Describe the morphology of the erythrocytes.
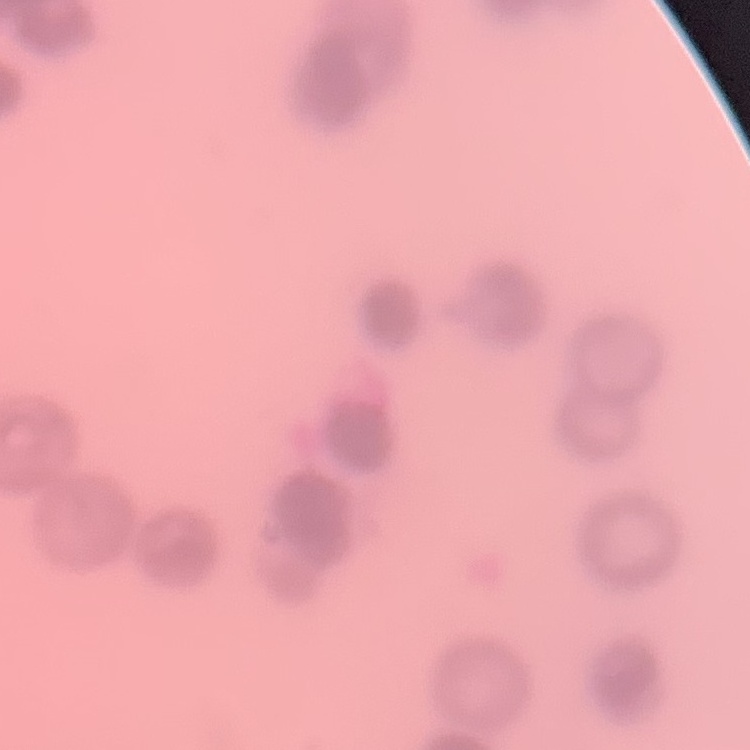

Rouleaux formation.

image_type: one tile cut from a larger photomicrograph
stain: Field's or Giemsa
preparation: thin blood smear